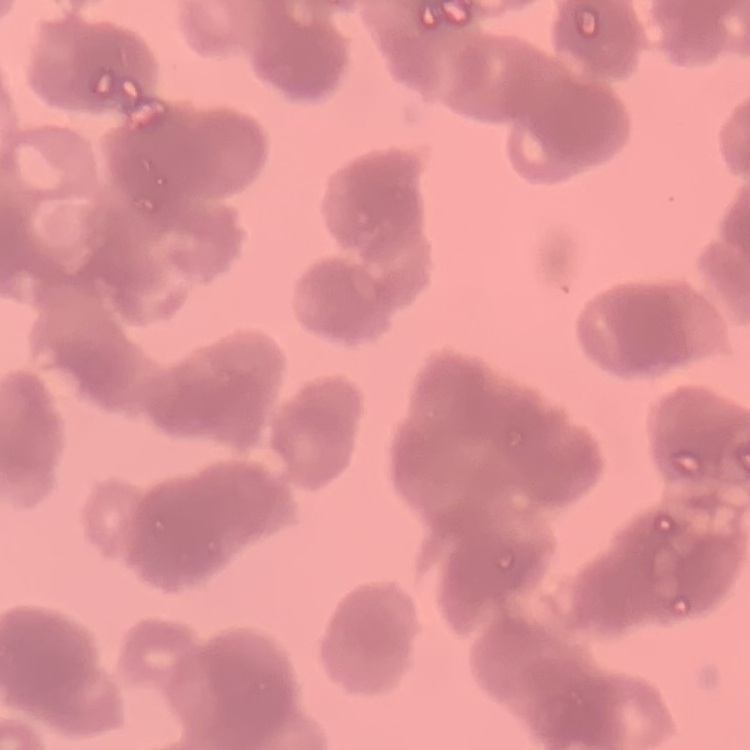
erythrocyte morphology = rouleaux formation
stain = Field's or Giemsa
preparation = thin peripheral smear
image type = one tile cut from a larger photomicrograph